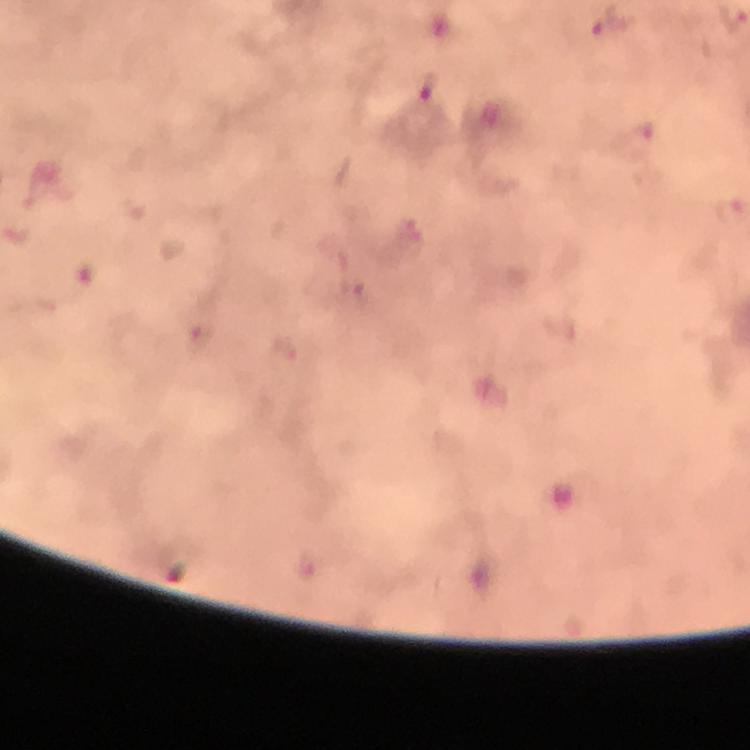

Approximate centers as [x, y] in pixels.
Summary:
  - Plasmodium parasite locations: [611, 25], [430, 93], [729, 208]
  - Immersion oil: used
  - Image size: 750×750 pixels
  - Capture: smartphone mounted on the microscope
  - Context: from a malaria diagnostic workup
  - Stain: Giemsa
  - Magnification: 100x
  - Cropped from: one field of view
  - Preparation: thick smear